Classify this cell by malaria status.
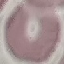

Uninfected.

Summary:
  - Stain: Giemsa
  - Capture: smartphone camera at the microscope eyepiece
  - Image type: automatically extracted cell patch, resized to 64 × 64 pixels
  - Preparation: thin blood film